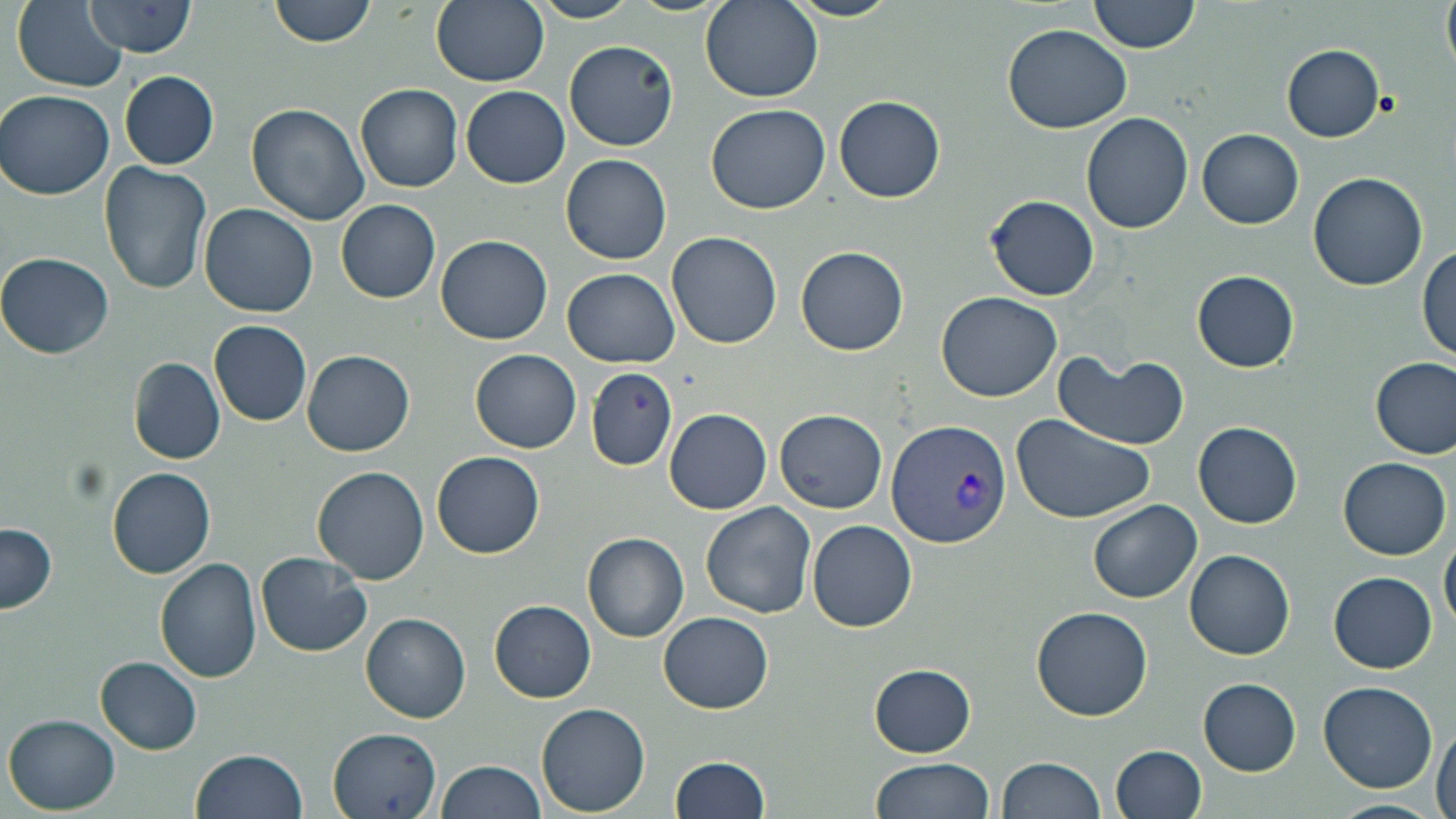 Approximate bounding boxes as (x1, y1, x2, y2) in pixels. Uninfected red blood cell locations: (269, 0, 377, 48), (529, 0, 640, 23), (699, 0, 822, 103), (784, 0, 903, 22), (1088, 0, 1200, 53), (1441, 0, 1456, 80), (82, 1, 198, 57), (430, 1, 548, 87), (12, 2, 127, 92), (1002, 24, 1131, 132), (564, 40, 678, 151), (1281, 45, 1385, 142), (120, 70, 219, 170), (354, 84, 463, 193), (461, 86, 570, 189), (1, 90, 116, 200), (833, 95, 945, 203), (246, 102, 370, 226), (705, 103, 831, 215), (1080, 113, 1193, 234), (1197, 129, 1303, 229), (559, 154, 672, 264), (97, 162, 214, 298), (1307, 172, 1430, 291), (985, 195, 1098, 302), (335, 199, 440, 303), (199, 202, 318, 317), (666, 231, 782, 350), (435, 236, 553, 345), (795, 245, 908, 356), (1416, 247, 1456, 363), (0, 253, 116, 358), (562, 268, 680, 367), (1192, 270, 1298, 372), (936, 292, 1062, 402), (209, 320, 311, 426), (470, 349, 581, 453), (302, 350, 414, 457), (1052, 350, 1191, 451), (128, 357, 225, 465), (1371, 357, 1456, 458), (585, 366, 678, 470), (663, 408, 773, 515), (774, 409, 888, 513), (1011, 415, 1156, 525), (1193, 421, 1302, 529), (432, 450, 545, 558), (1339, 456, 1451, 560), (106, 466, 217, 579), (312, 466, 430, 584), (1088, 499, 1202, 603), (700, 503, 817, 619), (808, 520, 917, 633), (0, 523, 57, 613), (582, 532, 689, 643), (1439, 534, 1456, 635), (1185, 550, 1295, 660), (255, 552, 372, 659), (154, 556, 262, 683), (1329, 572, 1436, 674), (489, 600, 596, 702), (1031, 607, 1154, 721), (360, 611, 471, 723), (657, 611, 772, 713), (95, 657, 202, 755), (869, 664, 976, 758), (1198, 677, 1301, 776), (1318, 681, 1438, 793), (536, 703, 650, 815), (3, 713, 121, 816), (1432, 720, 1456, 819), (327, 727, 441, 818), (1109, 745, 1206, 819), (190, 749, 307, 818), (670, 757, 769, 818), (872, 757, 994, 819), (997, 757, 1106, 818), (435, 759, 544, 819), (1330, 798, 1444, 819). Plasmodium vivax-infected red blood cell locations: (887, 419, 1013, 549). Slide-level diagnosis: Plasmodium vivax. Thin blood film. May-Grünwald-Giemsa stain. 1000x magnification. Light microscopy. Image is 1456×819 pixels. Single field of view.